Assess this cell for malaria.
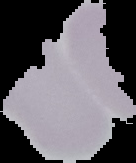

It is uninfected.

Segmented cell region on a black background. From a thin blood film. Image is 136×163 pixels.